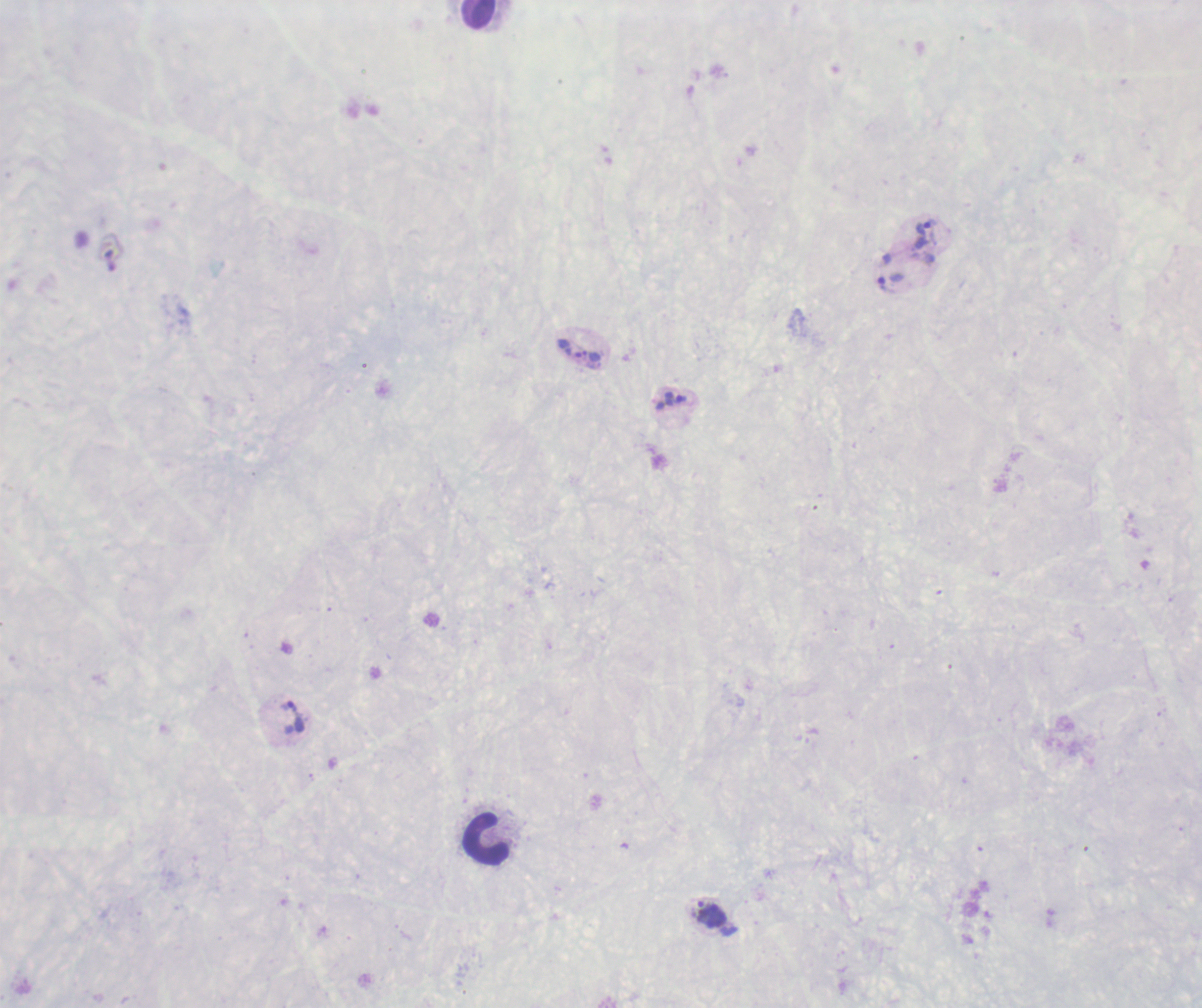

coordinate format = approximate centers as [x, y] in pixels
trophozoite locations = [926, 233], [891, 283], [591, 356], [675, 400], [292, 717], [712, 913]
leukocyte locations = [478, 14], [487, 840]
magnification = 100x
result = positive for Plasmodium parasites
background quality = unsatisfactory
image size = 1202×1008 pixels
coloration quality = bad
field of view = single
context = previously used in an actual diagnosis
preparation = thick blood smear
stain = Romanowsky